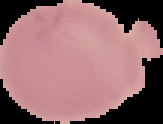
image type = segmented cell region with the area outside set to black
image size = 163×124 pixels
preparation = thin blood smear
malaria status = uninfected